Identify the preparation type.
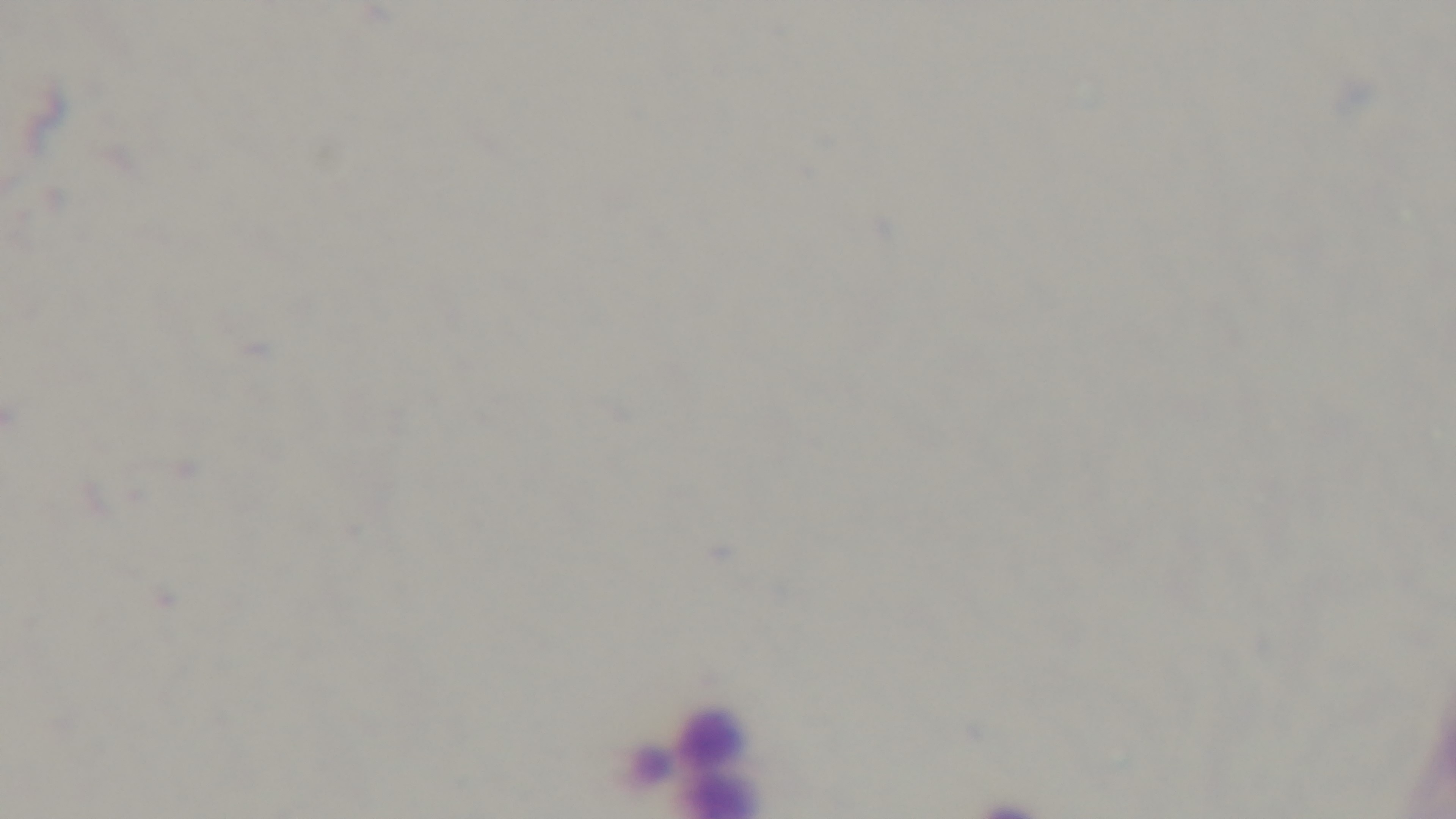

It is a thick blood film.

Mounted 4K digital camera. Malaria status: negative. 100x oil-immersion objective. Photomicrograph. Giemsa-stained. Single field of view.